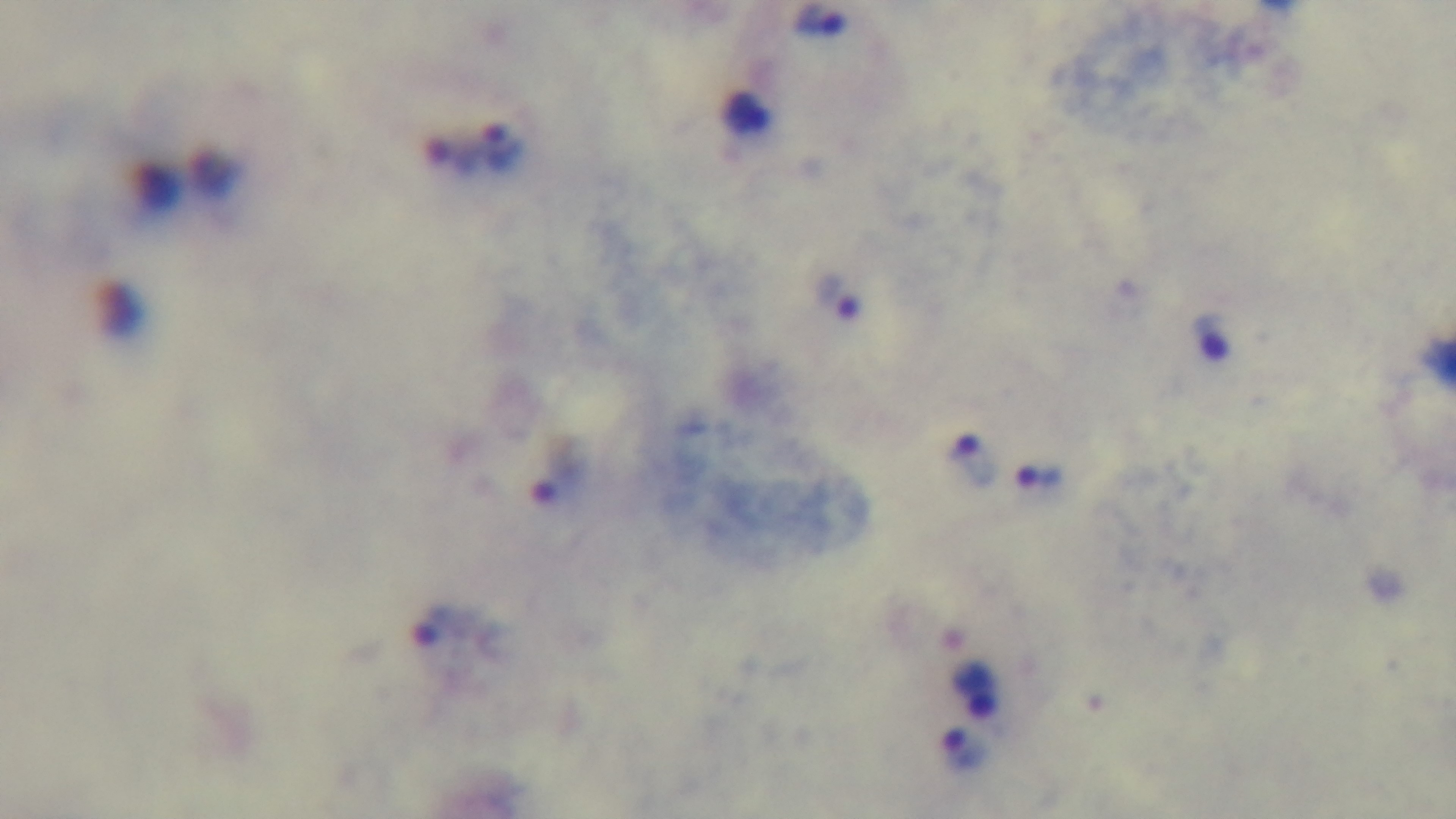
Summary:
  - Capture: mounted 4K digital camera
  - Malaria status: infected
  - Preparation: thick
  - Stain: Giemsa
  - Objective: 100x oil immersion
  - Modality: light microscopy
  - Field of view: one from the slide